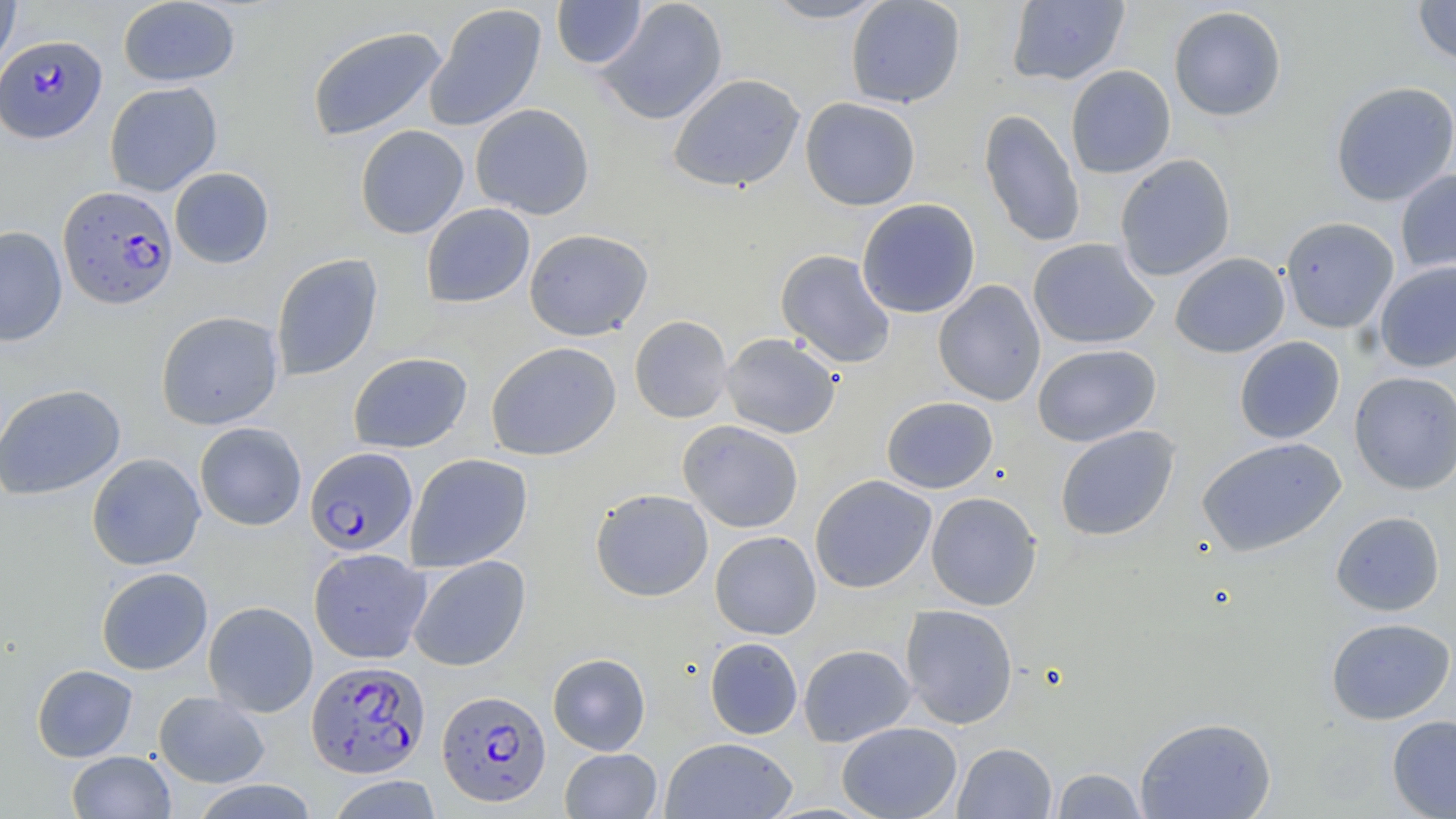
Summary:
  - Coordinate format: approximate bounding boxes as named x1/y1/x2/y2 corners in pixels
  - Uninfected red blood cell locations: (x1=0, y1=0, x2=21, y2=76), (x1=118, y1=0, x2=241, y2=87), (x1=551, y1=0, x2=647, y2=69), (x1=760, y1=0, x2=890, y2=24), (x1=846, y1=0, x2=965, y2=108), (x1=1007, y1=0, x2=1129, y2=86), (x1=1412, y1=0, x2=1456, y2=67), (x1=597, y1=1, x2=728, y2=125), (x1=425, y1=3, x2=547, y2=132), (x1=1168, y1=5, x2=1287, y2=122), (x1=306, y1=25, x2=448, y2=142), (x1=1065, y1=65, x2=1176, y2=178), (x1=668, y1=73, x2=805, y2=193), (x1=1330, y1=81, x2=1456, y2=207), (x1=104, y1=82, x2=222, y2=196), (x1=800, y1=97, x2=921, y2=210), (x1=470, y1=103, x2=595, y2=220), (x1=979, y1=109, x2=1085, y2=248), (x1=355, y1=119, x2=594, y2=228), (x1=355, y1=125, x2=469, y2=239), (x1=1115, y1=154, x2=1235, y2=281), (x1=169, y1=167, x2=275, y2=268), (x1=1395, y1=168, x2=1456, y2=277), (x1=857, y1=198, x2=981, y2=318), (x1=421, y1=203, x2=535, y2=308), (x1=1280, y1=216, x2=1399, y2=333), (x1=0, y1=226, x2=67, y2=347), (x1=524, y1=228, x2=653, y2=341), (x1=1028, y1=238, x2=1159, y2=349), (x1=776, y1=249, x2=896, y2=368), (x1=1170, y1=252, x2=1290, y2=358), (x1=271, y1=254, x2=383, y2=381), (x1=1375, y1=261, x2=1456, y2=372), (x1=933, y1=280, x2=1046, y2=406), (x1=156, y1=311, x2=283, y2=430), (x1=629, y1=315, x2=733, y2=423), (x1=721, y1=333, x2=841, y2=439), (x1=1234, y1=336, x2=1345, y2=443), (x1=485, y1=341, x2=621, y2=461), (x1=1032, y1=343, x2=1161, y2=447), (x1=348, y1=352, x2=472, y2=453), (x1=1349, y1=370, x2=1456, y2=494), (x1=0, y1=383, x2=126, y2=500), (x1=881, y1=396, x2=998, y2=494), (x1=678, y1=420, x2=804, y2=533), (x1=195, y1=422, x2=307, y2=530), (x1=1054, y1=425, x2=1179, y2=541), (x1=1196, y1=437, x2=1346, y2=557), (x1=86, y1=453, x2=206, y2=570), (x1=405, y1=453, x2=533, y2=571), (x1=810, y1=474, x2=936, y2=594), (x1=590, y1=488, x2=713, y2=601), (x1=926, y1=491, x2=1042, y2=611), (x1=1331, y1=511, x2=1445, y2=616), (x1=710, y1=531, x2=821, y2=640), (x1=308, y1=548, x2=431, y2=663), (x1=408, y1=555, x2=531, y2=671), (x1=96, y1=567, x2=212, y2=675), (x1=203, y1=601, x2=318, y2=717), (x1=900, y1=604, x2=1018, y2=729), (x1=1325, y1=617, x2=1456, y2=725), (x1=705, y1=637, x2=803, y2=739), (x1=798, y1=644, x2=916, y2=747), (x1=547, y1=652, x2=651, y2=755), (x1=31, y1=664, x2=138, y2=762), (x1=153, y1=691, x2=270, y2=788), (x1=1387, y1=714, x2=1456, y2=818), (x1=1134, y1=715, x2=1277, y2=818), (x1=836, y1=721, x2=962, y2=819), (x1=660, y1=737, x2=798, y2=819), (x1=953, y1=742, x2=1057, y2=818), (x1=559, y1=748, x2=662, y2=819), (x1=67, y1=751, x2=176, y2=818), (x1=1051, y1=767, x2=1149, y2=819), (x1=326, y1=774, x2=444, y2=818), (x1=189, y1=780, x2=320, y2=818)
  - Plasmodium falciparum-infected red blood cell locations: (x1=0, y1=35, x2=107, y2=144), (x1=58, y1=186, x2=177, y2=309), (x1=304, y1=447, x2=417, y2=556), (x1=305, y1=659, x2=431, y2=778), (x1=437, y1=690, x2=551, y2=806)
  - Slide-level diagnosis: Plasmodium falciparum
  - Preparation: thin blood film
  - Field of view: single
  - Image size: 1456×819 pixels
  - Magnification: 1000x
  - Modality: light microscopy
  - Stain: May-Grünwald-Giemsa